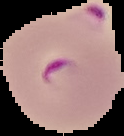

Summary:
  - Malaria status: parasitized
  - Preparation: thin blood smear
  - Image type: segmented cell region on a black background
  - Image size: 124×136 pixels